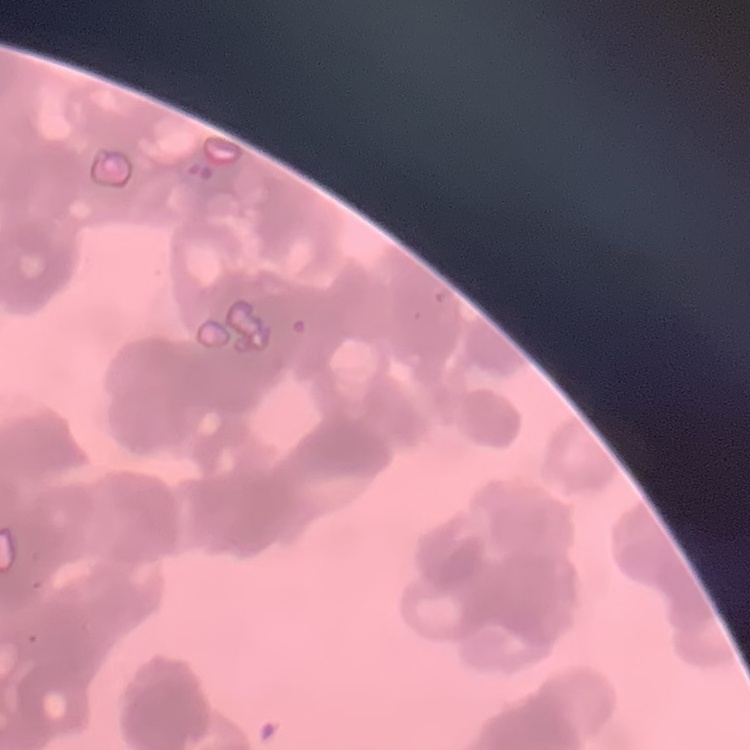
{
  "erythrocyte_morphology": "rouleaux formation",
  "stain": "Field's or Giemsa",
  "image_type": "one tile cut from a larger photomicrograph",
  "preparation": "thin peripheral smear"
}